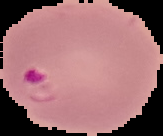

result = malaria parasites identified
preparation = thin blood film
image type = segmented cell region on a black background
image size = 163×136 pixels